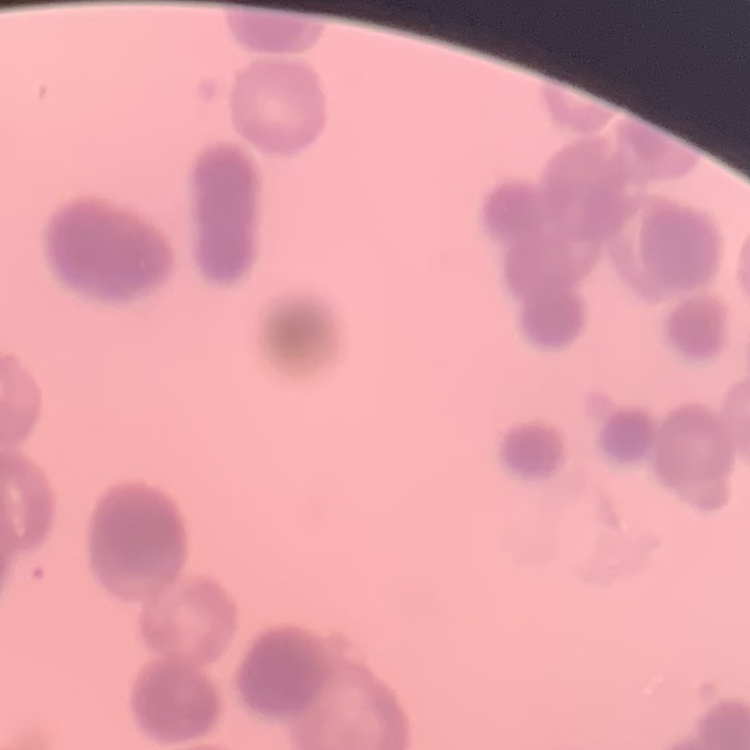

Summary:
  - Red blood cell morphology: rouleaux formation
  - Image type: one tile cut from a larger photomicrograph
  - Stain: Field's or Giemsa
  - Preparation: thin blood film